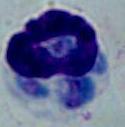
identification = leukocyte
modality = micrograph
magnification = 1000x